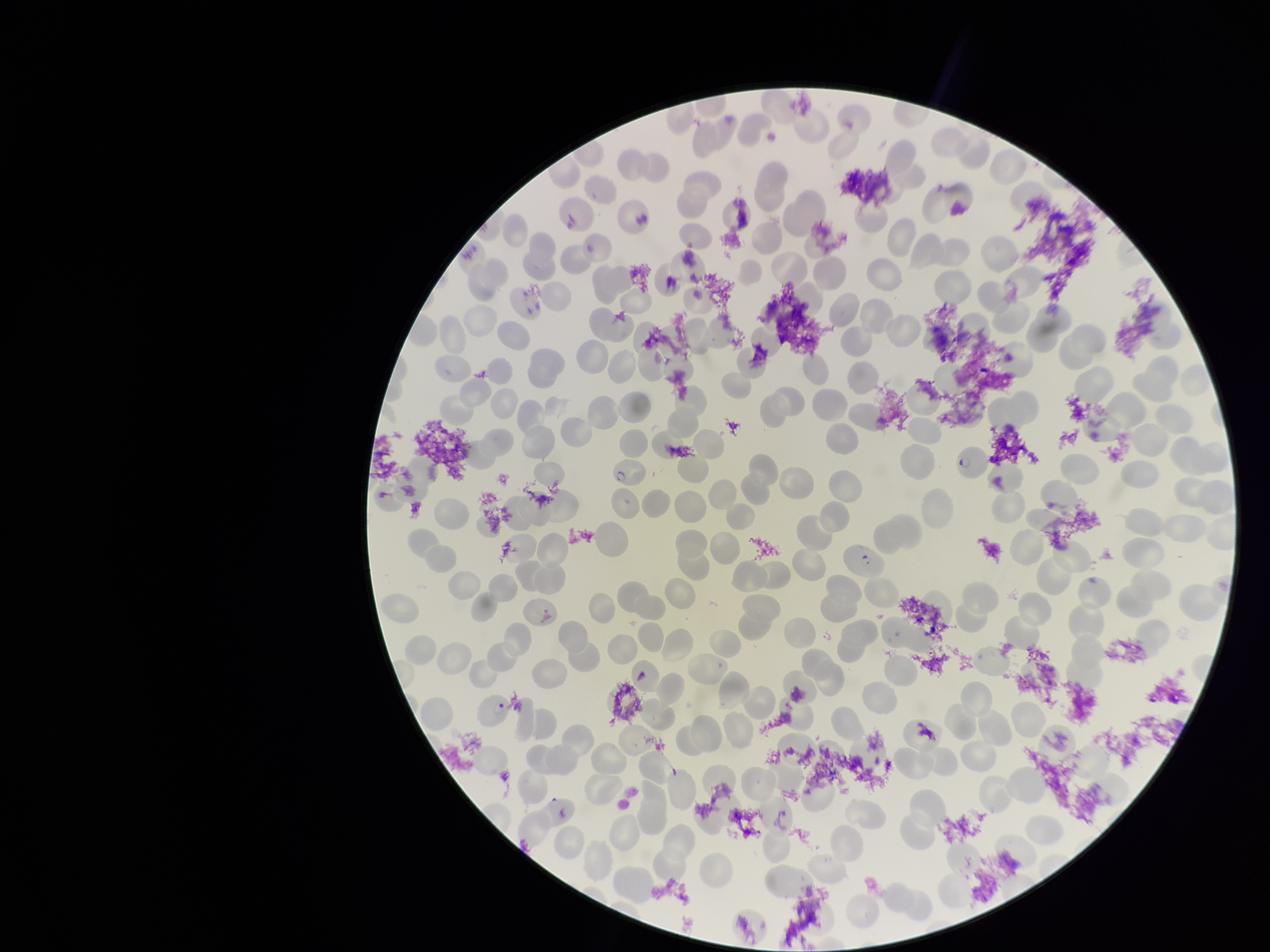

image size = 1270×952 pixels
patient malaria status = positive
field of view = one from this slide
parasitized red blood cell count = 3
preparation = thin blood smear
red blood cell count = 240
species reported for this patient = Plasmodium falciparum
parasitized red blood cells = identified
capture = smartphone photograph through the microscope eyepiece
stain = Giemsa